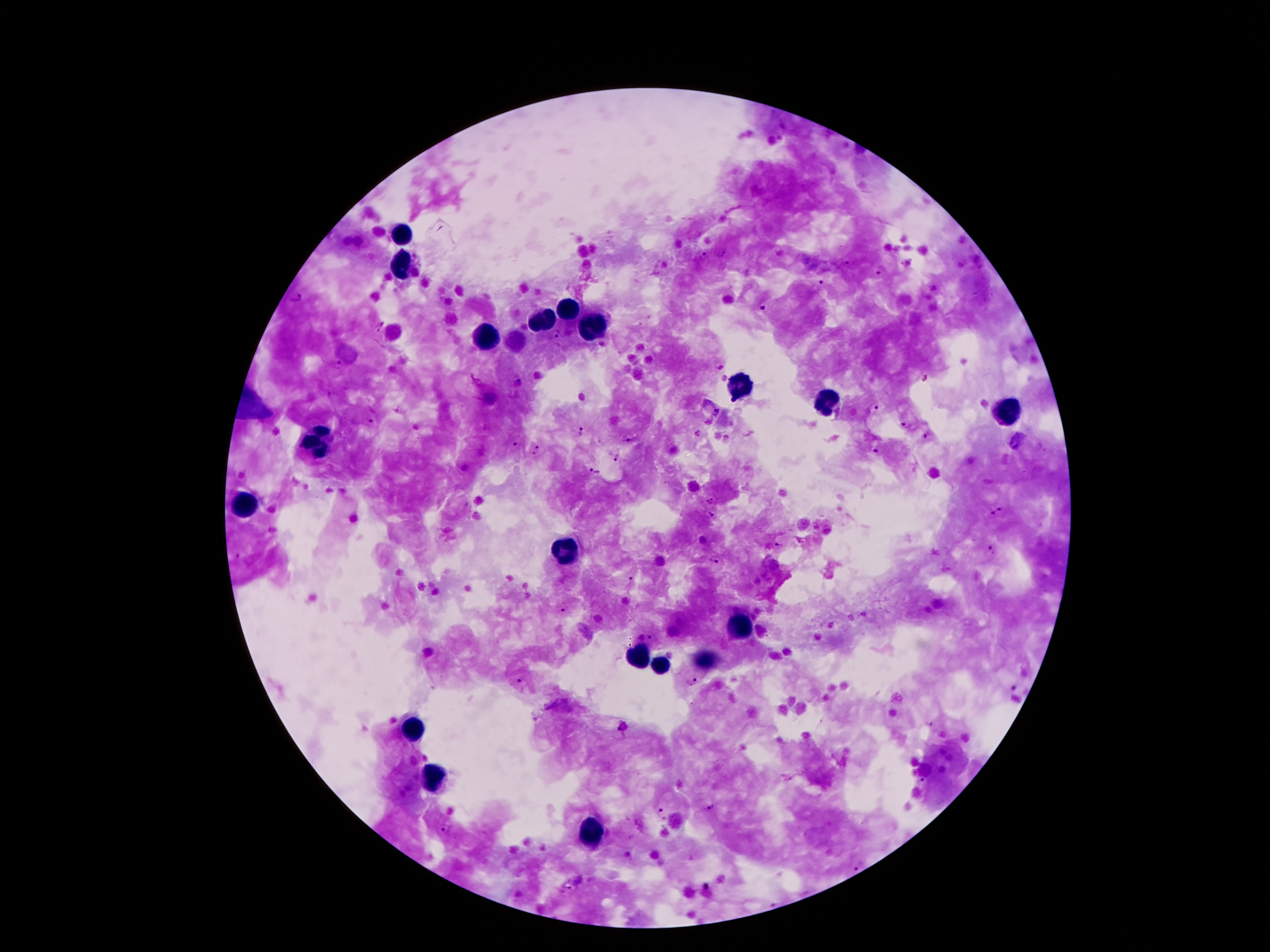

Approximate centers as [x, y] in pixels.
Summary:
  - Malaria parasite locations: [702, 256], [849, 260], [879, 268], [820, 282], [296, 296], [761, 306], [378, 325], [555, 334], [334, 366], [924, 377], [519, 385], [875, 407], [718, 412], [371, 421], [904, 423], [580, 431], [927, 436], [630, 439], [515, 445], [535, 449], [874, 451], [618, 458], [596, 470], [712, 500], [999, 512], [714, 516], [780, 545], [990, 551], [714, 560], [631, 578], [564, 610], [649, 637], [691, 680], [519, 681], [1013, 689], [930, 723], [625, 728], [919, 782], [708, 809], [659, 812], [442, 830], [856, 866], [572, 883], [708, 894]
  - Leukocyte locations: [401, 234], [403, 267], [567, 311], [544, 322], [590, 324], [489, 337], [739, 385], [825, 400], [1008, 412], [317, 442], [244, 505], [562, 551], [737, 625], [636, 656], [659, 666], [705, 666], [411, 727], [434, 776], [588, 834]
  - Field of view: one from this slide
  - Preparation: thick blood smear
  - Patient malaria status: positive for Plasmodium falciparum
  - Stain: Giemsa
  - Capture: smartphone through the microscope eyepiece
  - Magnification: 100x
  - Image size: 1270×952 pixels